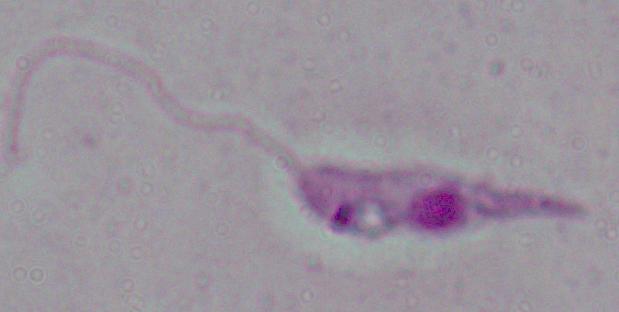
identification: Leishmania
modality: photomicrograph
magnification: 1000x